Report the malaria status of this cell.
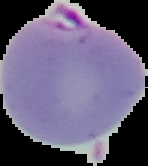

It is parasitized.

image_type: segmented cell region with the area outside set to black
preparation: thin blood film
image_size: 148×166 pixels